Identify the blood parasite species.
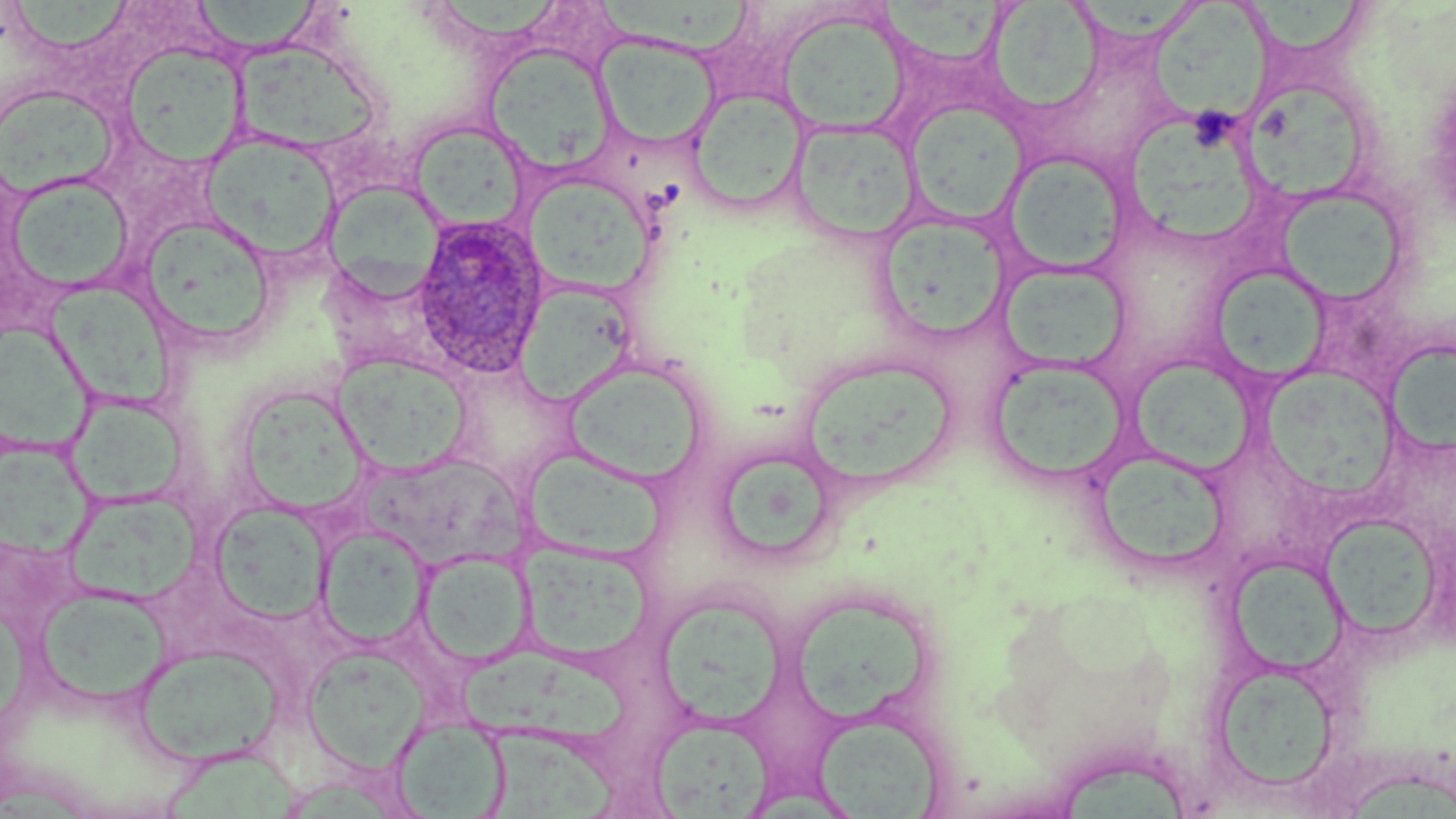

Plasmodium ovale.

Summary:
  - Coordinate format: approximate bounding boxes as [x1, y1, x2, y2] in pixels
  - Plasmodium ovale-infected red blood cell locations: [412, 215, 552, 381]
  - Uninfected red blood cell locations: [11, 0, 137, 53], [196, 0, 327, 60], [442, 0, 563, 45], [982, 0, 1105, 119], [1079, 0, 1199, 45], [1252, 0, 1365, 58], [590, 2, 756, 61], [1152, 2, 1275, 128], [776, 10, 910, 137], [595, 34, 720, 149], [236, 39, 386, 156], [118, 44, 247, 168], [484, 45, 614, 174], [1, 85, 121, 200], [686, 88, 810, 214], [1244, 90, 1370, 203], [906, 100, 1028, 226], [1133, 118, 1259, 243], [790, 120, 921, 243], [406, 121, 531, 235], [202, 131, 340, 263], [1004, 151, 1130, 275], [3, 173, 135, 296], [523, 173, 656, 298], [322, 181, 446, 302], [1279, 194, 1406, 308], [876, 214, 1012, 344], [138, 216, 278, 351], [997, 261, 1131, 374], [1216, 269, 1329, 383], [514, 282, 636, 408], [48, 287, 176, 410], [1, 326, 105, 454], [1384, 340, 1456, 459], [332, 351, 474, 476], [798, 353, 956, 491], [1126, 356, 1256, 474], [987, 357, 1131, 486], [563, 361, 708, 485], [1258, 365, 1406, 505], [240, 389, 373, 521], [66, 394, 192, 509], [0, 447, 102, 564], [523, 447, 666, 562], [1090, 449, 1231, 573], [358, 452, 535, 572], [727, 460, 838, 560], [66, 491, 200, 605], [208, 501, 332, 624], [1318, 513, 1444, 644], [317, 525, 431, 648], [521, 544, 654, 663], [417, 548, 533, 668], [1226, 553, 1350, 676], [34, 586, 171, 709], [653, 595, 787, 727], [788, 601, 933, 725], [134, 642, 284, 765], [303, 645, 429, 773], [457, 655, 641, 742], [1209, 661, 1341, 796], [812, 712, 945, 817], [648, 714, 776, 817], [390, 719, 510, 818], [495, 729, 630, 818], [162, 749, 304, 816], [1060, 761, 1192, 819], [1350, 769, 1456, 819]
  - Preparation: thin blood film
  - Image size: 1456×819 pixels
  - Field of view: one of a larger specimen
  - Modality: light microscopy
  - Stain: May-Grünwald-Giemsa
  - Magnification: 1000x